Describe the morphology of the erythrocytes.
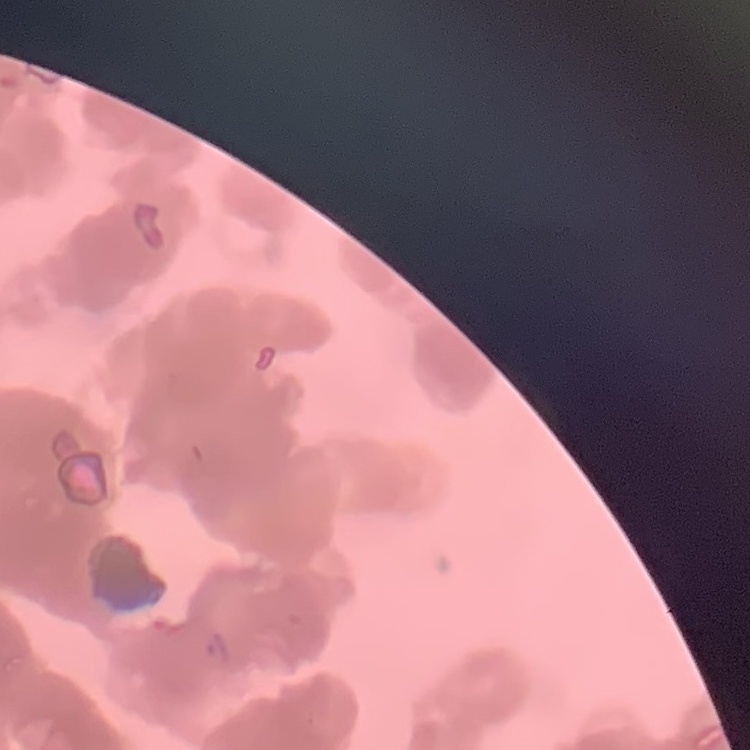

Rouleaux formation.

Summary:
  - Preparation: thin peripheral smear
  - Stain: Field's or Giemsa
  - Image type: square crop of a larger photomicrograph